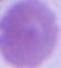

A red blood cell is seen. 1000x magnification. Photomicrograph.